Locate and identify every blood parasite.
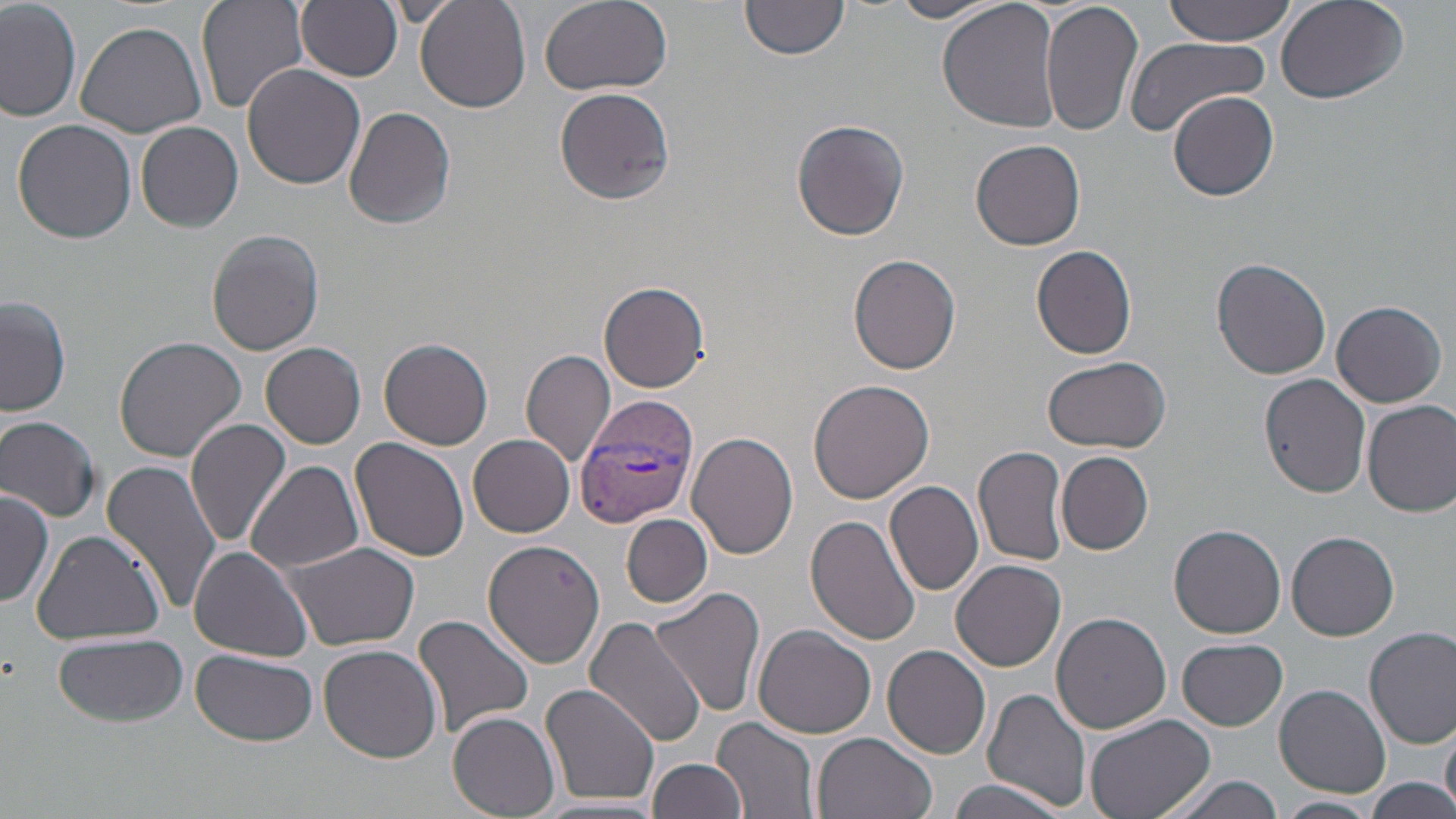

Approximate bounding boxes as (x1,y1)-(x2,y2) corner pairs in pixels.
Plasmodium vivax-infected red blood cells: (576,394)-(695,525).
No Plasmodium falciparum, Plasmodium ovale, Plasmodium malariae, Babesia divergens, or Trypanosoma brucei observed.

Summary:
  - Uninfected red blood cell locations: (197,0)-(309,115), (416,0)-(531,114), (538,0)-(673,95), (937,0)-(1064,135), (1040,0)-(1145,138), (1159,0)-(1301,46), (1273,0)-(1410,105), (0,1)-(80,121), (297,1)-(402,80), (887,1)-(1000,23), (739,2)-(848,63), (75,22)-(207,138), (1124,35)-(1271,138), (241,61)-(365,189), (554,86)-(676,207), (1169,91)-(1279,201), (343,104)-(457,230), (12,119)-(138,245), (791,119)-(909,243), (136,121)-(243,233), (971,139)-(1086,251), (206,229)-(325,355), (1031,245)-(1138,359), (848,253)-(962,375), (1212,258)-(1333,379), (598,281)-(712,393), (2,295)-(71,418), (1331,300)-(1446,407), (114,335)-(248,463), (380,338)-(493,451), (261,342)-(366,449), (521,349)-(616,469), (1042,355)-(1172,454), (1261,375)-(1372,496), (806,378)-(933,504), (1363,399)-(1456,517), (0,415)-(101,521), (186,417)-(293,547), (687,432)-(798,559), (467,433)-(575,537), (350,438)-(471,565), (974,445)-(1070,568), (1057,451)-(1154,555), (103,459)-(223,618), (245,461)-(364,573), (884,479)-(985,597), (1,488)-(53,610), (621,513)-(713,608), (805,514)-(922,646), (1170,524)-(1286,638), (31,529)-(167,644), (1286,531)-(1400,641), (480,538)-(605,665), (283,541)-(420,650), (191,546)-(313,662), (951,559)-(1066,672), (650,583)-(765,719), (1052,612)-(1173,734), (413,613)-(535,743), (585,615)-(706,745), (752,625)-(876,738), (1364,627)-(1456,749), (56,634)-(189,727), (1177,638)-(1287,730), (319,643)-(442,762), (883,645)-(991,760), (191,648)-(319,746), (539,682)-(661,807), (1275,684)-(1390,797), (983,688)-(1094,811), (448,712)-(559,817), (1084,713)-(1215,819), (714,718)-(822,818), (1443,719)-(1456,813), (811,733)-(937,819), (647,757)-(748,819), (1152,772)-(1288,819), (944,776)-(1072,818), (1364,777)-(1456,818), (1274,795)-(1379,819)
  - Slide-level diagnosis: Plasmodium vivax
  - Magnification: 1000x
  - Modality: optical microscopy
  - Stain: May-Grünwald-Giemsa
  - Image size: 1456×819 pixels
  - Field of view: single
  - Preparation: thin blood film